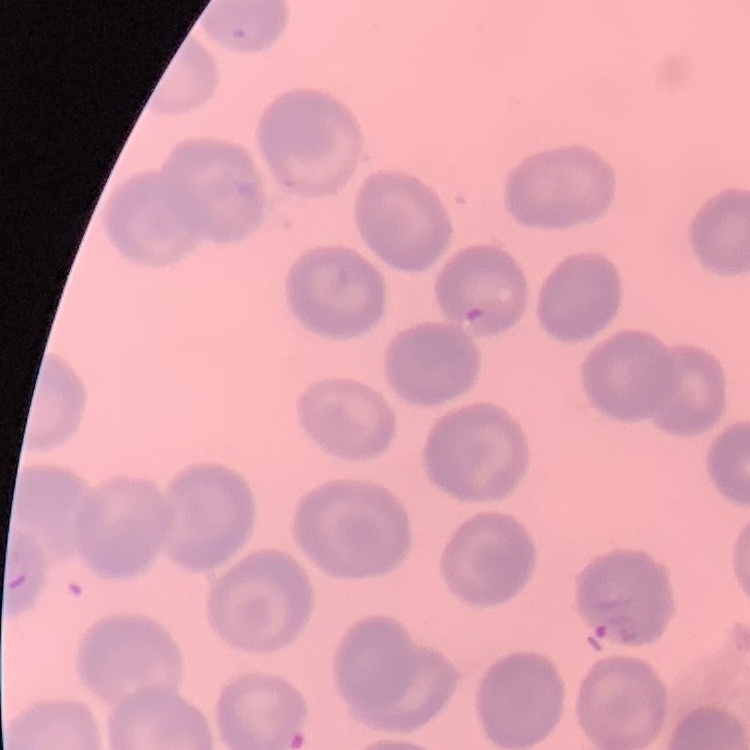

The erythrocytes show no rouleaux formation. Thin blood smear. Stained with either Field's or Giemsa. One tile cut from a larger photomicrograph.